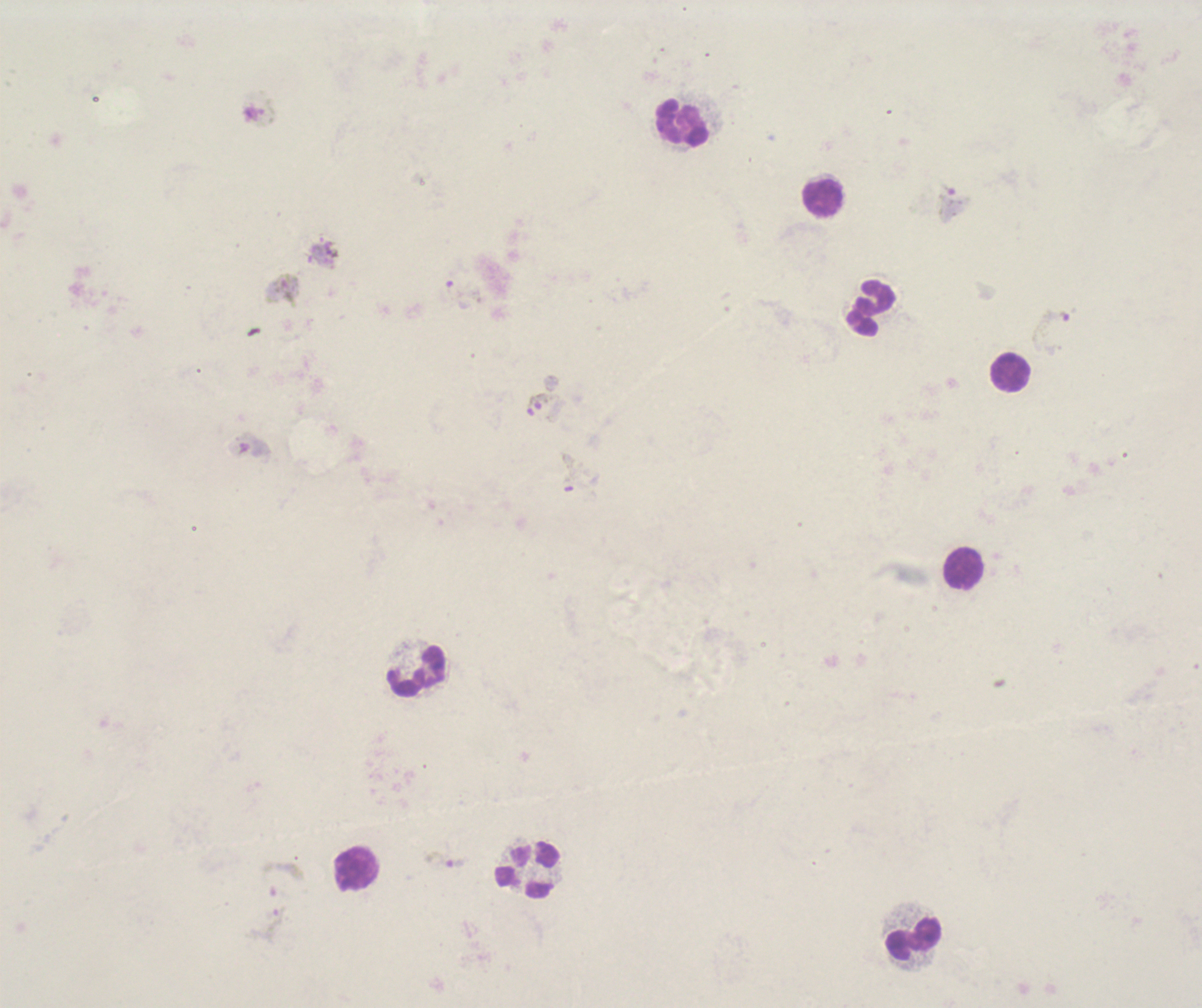

Approximate centers as {x, y} in pixels.
Summary:
  - Leukocyte locations: {682, 123}, {822, 197}, {871, 308}, {1011, 372}, {964, 568}, {417, 671}, {357, 868}, {527, 869}, {913, 938}
  - Gametocyte locations: {260, 107}, {951, 202}, {284, 290}, {462, 294}, {1051, 322}, {542, 401}, {253, 445}, {569, 472}, {446, 860}, {284, 879}, {275, 923}
  - Result: Plasmodium parasites detected
  - Coloration quality: bad
  - Image size: 1202×1008 pixels
  - Context: previously used in an actual diagnosis
  - Magnification: 100x
  - Stain: Romanowsky
  - Field of view: one from this slide
  - Background quality: unsatisfactory
  - Preparation: thick smear of blood